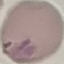
Result: malaria parasites identified. Cell patch, automatically extracted from a larger field of view and resized to 64 × 64 pixels. Acquired by smartphone through the microscope eyepiece. Giemsa stain. Thin blood film.